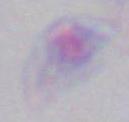

Summary:
  - Modality: photomicrograph
  - Identification: Toxoplasma gondii
  - Magnification: 1000x